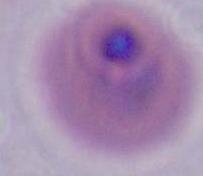
A Plasmodium parasite is shown. Photomicrograph. 400x or 1000x magnification.